State the blood parasite species.
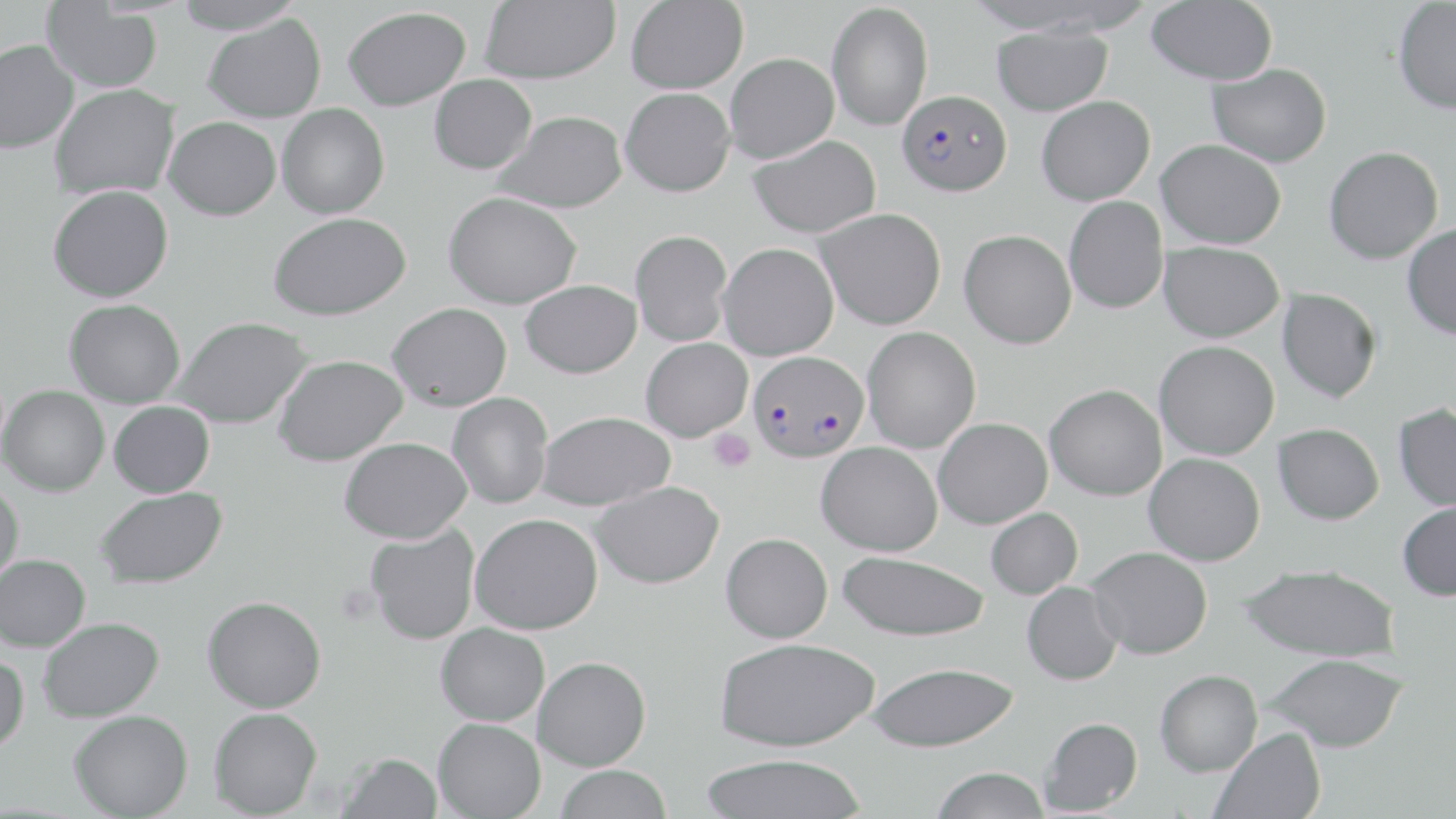
Plasmodium falciparum.

uninfected red blood cell locations = approximate bounding boxes as (x1, y1, x2, y2) in pixels: (172, 0, 305, 34), (480, 0, 620, 84), (626, 0, 748, 93), (1392, 0, 1456, 114), (1146, 1, 1278, 85), (42, 2, 163, 92), (826, 2, 933, 131), (343, 7, 471, 110), (203, 13, 326, 123), (991, 24, 1113, 116), (0, 40, 79, 153), (725, 52, 839, 163), (1207, 63, 1331, 166), (429, 74, 536, 174), (49, 84, 180, 201), (620, 87, 735, 196), (1037, 95, 1155, 205), (276, 104, 389, 218), (495, 110, 627, 213), (163, 116, 281, 220), (747, 135, 882, 237), (1156, 139, 1285, 248), (1323, 146, 1444, 264), (48, 184, 173, 302), (443, 191, 581, 309), (1064, 197, 1168, 313), (816, 207, 946, 329), (269, 212, 410, 320), (1402, 222, 1456, 340), (630, 229, 733, 346), (959, 229, 1077, 349), (1159, 241, 1284, 342), (718, 243, 838, 360), (520, 279, 641, 378), (1277, 288, 1381, 403), (64, 299, 185, 407), (387, 302, 512, 411), (172, 316, 312, 429), (862, 326, 981, 453), (641, 337, 753, 441), (1154, 341, 1279, 460), (272, 354, 408, 466), (1044, 383, 1167, 500), (1, 385, 109, 496), (447, 393, 553, 509), (108, 401, 214, 497), (1393, 404, 1456, 512), (536, 410, 675, 510), (933, 417, 1052, 528), (1273, 423, 1384, 524), (339, 437, 472, 543), (816, 441, 942, 556), (1144, 452, 1265, 565), (591, 481, 724, 589), (0, 482, 24, 586), (94, 487, 227, 588), (1397, 499, 1456, 601), (985, 507, 1083, 599), (470, 513, 603, 635), (364, 523, 480, 645), (721, 532, 833, 643), (1087, 546, 1212, 659), (838, 551, 989, 641), (0, 555, 90, 651), (1240, 563, 1400, 663), (1022, 582, 1123, 685), (202, 596, 326, 713), (38, 617, 165, 722), (435, 623, 549, 726), (715, 637, 879, 751), (0, 653, 29, 754), (1264, 653, 1407, 752), (533, 656, 651, 770), (866, 662, 1019, 752), (1154, 669, 1262, 776), (209, 707, 322, 818), (69, 709, 193, 818), (1040, 717, 1142, 815), (432, 718, 545, 819), (1209, 727, 1326, 819), (337, 752, 442, 818), (698, 753, 868, 818), (555, 765, 672, 819), (930, 766, 1051, 819)
image size = 1456×819 pixels
Plasmodium falciparum-infected red blood cell locations = approximate bounding boxes as (x1, y1, x2, y2) in pixels: (896, 89, 1012, 195), (748, 350, 869, 462)
stain = May-Grünwald-Giemsa
preparation = thin blood smear
magnification = 1000x
modality = light microscopy
field of view = one of a larger specimen
platelet locations = approximate bounding boxes as (x1, y1, x2, y2) in pixels: (708, 429, 755, 473)